Locate every Plasmodium parasite.
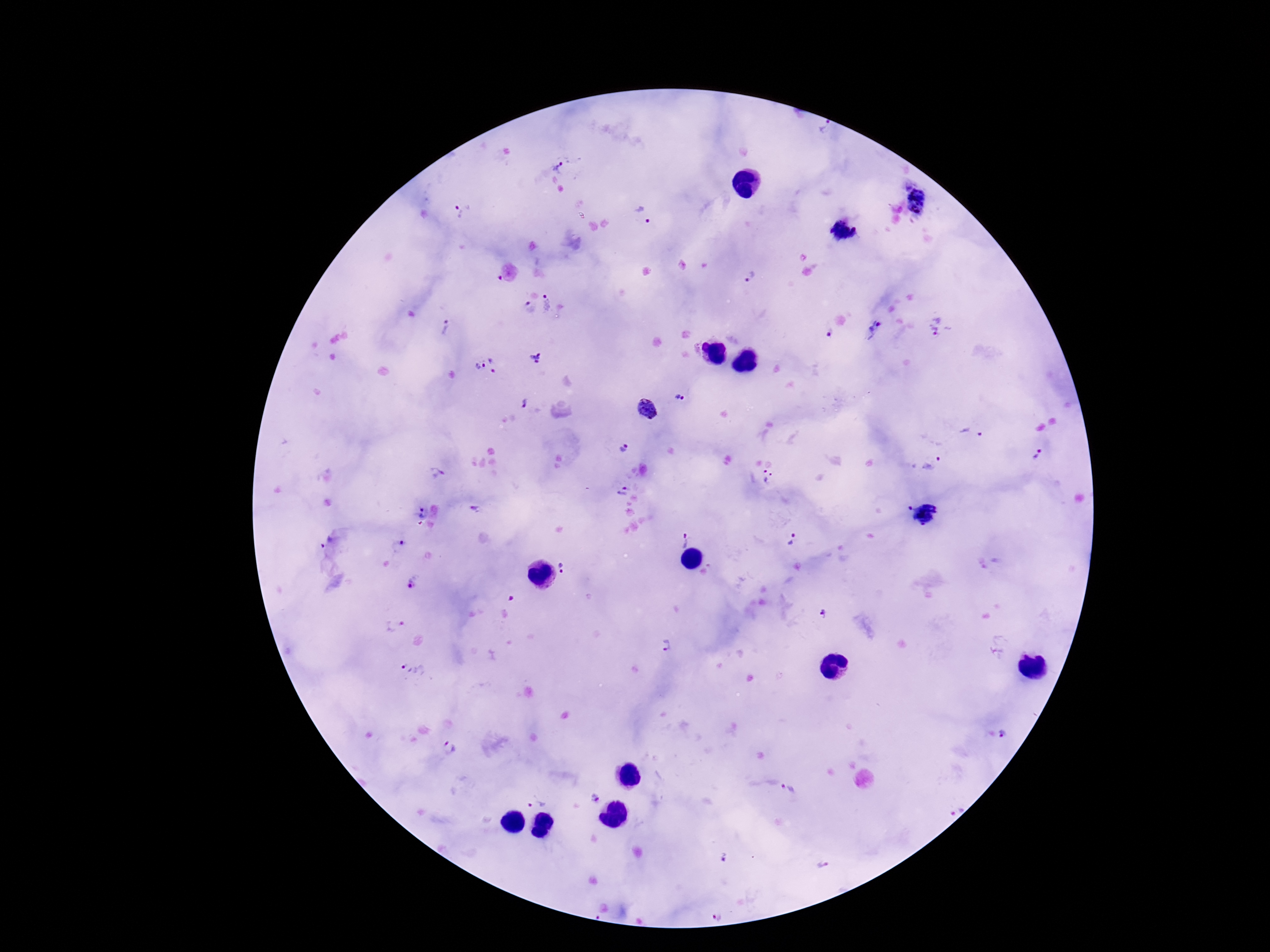

Approximate centers as (x, y) in pixels.
Plasmodium parasites: (558, 168), (918, 200), (459, 207), (643, 217), (844, 230), (750, 277), (548, 303), (530, 309), (940, 326), (447, 329), (875, 329), (829, 334), (535, 357), (495, 364), (478, 367), (682, 399), (523, 403), (647, 410), (972, 433), (622, 448), (1038, 453), (932, 462), (768, 476), (622, 491), (909, 507), (419, 513), (925, 513), (682, 538), (792, 539), (326, 541), (399, 546), (564, 566), (409, 583), (823, 613), (395, 626), (666, 645), (415, 671), (1004, 734), (450, 746), (788, 790), (595, 801), (536, 803), (952, 806), (724, 858), (823, 863), (716, 913).

Summary:
  - Field of view: single
  - Stain: Giemsa
  - Patient malaria status: positive
  - Preparation: thick peripheral-blood smear
  - Image size: 1270×952 pixels
  - Magnification: 100x
  - Capture: smartphone camera through the microscope eyepiece